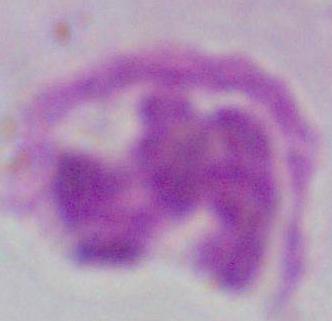 Captured at 1000x magnification. Photomicrograph. A white blood cell is shown.